Locate and identify every blood parasite.
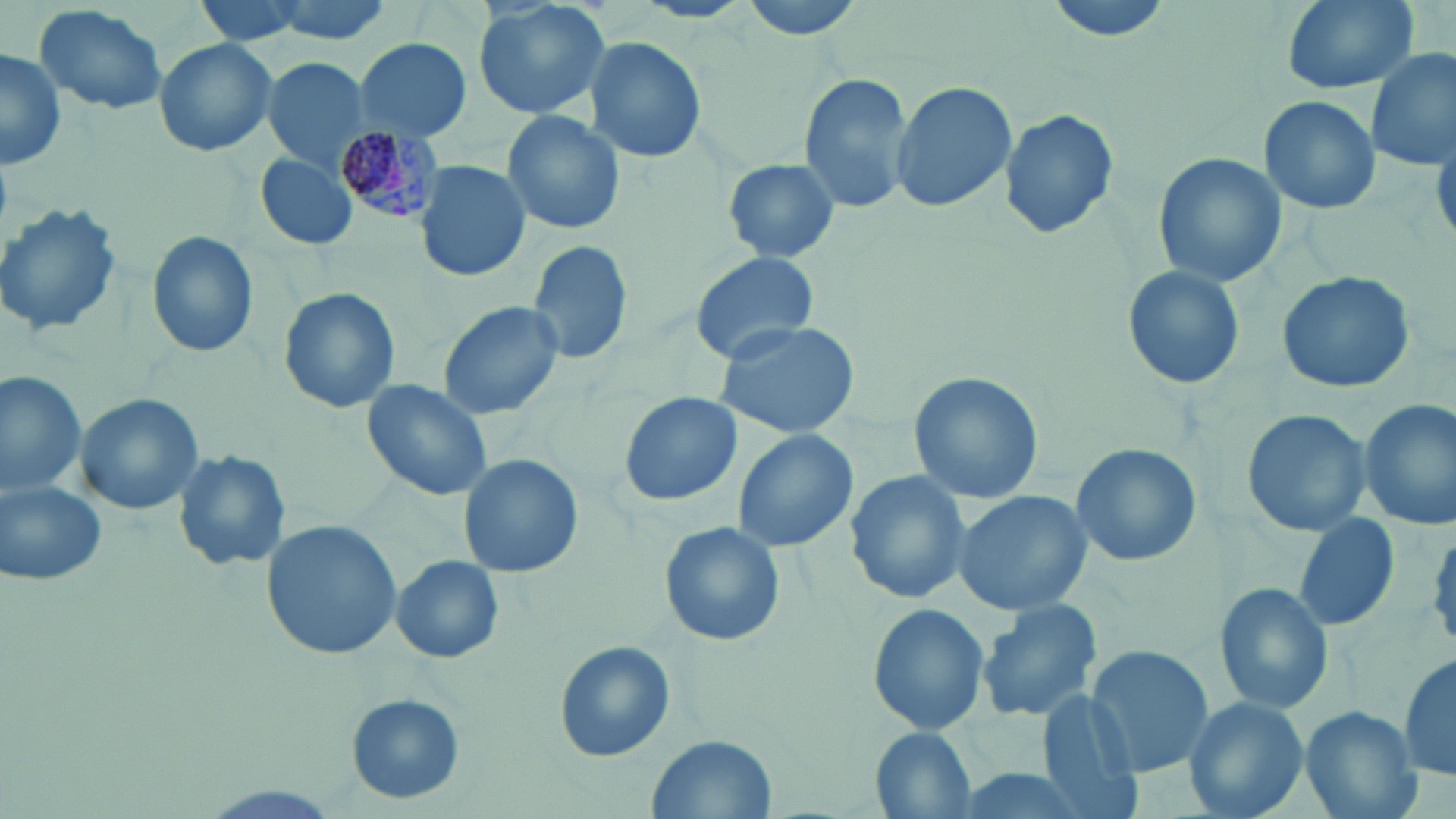
Approximate bounding boxes as (x1, y1, x2, y2) in pixels.
Plasmodium malariae-infected red blood cells: (333, 117, 444, 227).
No Plasmodium falciparum, Plasmodium ovale, Plasmodium vivax, Babesia divergens, or Trypanosoma brucei observed.

{
  "slide_level_diagnosis": "Plasmodium malariae",
  "modality": "light microscopy",
  "preparation": "thin blood smear",
  "image_size": "1456×819 pixels",
  "magnification": "1000x",
  "uninfected_red_blood_cell_locations": "approximate bounding boxes as (x1, y1, x2, y2) in pixels: (474, 0, 611, 120), (731, 0, 873, 41), (1038, 0, 1179, 44), (1277, 0, 1422, 94), (35, 4, 169, 114), (354, 31, 471, 134), (585, 35, 705, 164), (152, 37, 279, 156), (1364, 45, 1455, 173), (0, 47, 67, 171), (264, 57, 372, 168), (798, 72, 913, 217), (890, 80, 1017, 214), (1258, 94, 1381, 213), (999, 106, 1120, 241), (502, 110, 623, 236), (255, 150, 359, 251), (1152, 152, 1285, 290), (719, 156, 843, 267), (416, 160, 532, 282), (0, 202, 123, 338), (148, 231, 259, 358), (525, 240, 635, 368), (689, 251, 823, 365), (1124, 264, 1246, 389), (1276, 270, 1416, 395), (279, 288, 399, 411), (439, 300, 570, 421), (715, 318, 864, 440), (908, 371, 1041, 504), (1, 373, 88, 497), (359, 378, 494, 503), (75, 393, 205, 515), (619, 393, 742, 507), (1359, 399, 1455, 530), (1240, 407, 1371, 538), (730, 427, 859, 555), (1070, 443, 1202, 570), (172, 449, 292, 574), (457, 454, 583, 577), (844, 468, 974, 605), (0, 475, 110, 589), (951, 490, 1093, 616), (1292, 512, 1401, 637), (262, 519, 404, 661), (659, 521, 782, 646), (391, 554, 505, 664), (1214, 582, 1336, 714), (979, 600, 1103, 723), (866, 603, 990, 736), (555, 640, 674, 761), (1085, 646, 1213, 776), (1399, 648, 1454, 785), (1036, 690, 1144, 817), (348, 694, 464, 803), (1183, 697, 1309, 819), (1300, 706, 1420, 819), (871, 729, 978, 818), (648, 733, 776, 819), (938, 763, 1104, 819)",
  "field_of_view": "one of a larger specimen",
  "stain": "May-Grünwald-Giemsa"
}